Assess this cell for malaria.
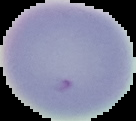
It is uninfected.

Summary:
  - Preparation: thin blood smear
  - Image type: segmented cell region on a black background
  - Image size: 136×121 pixels